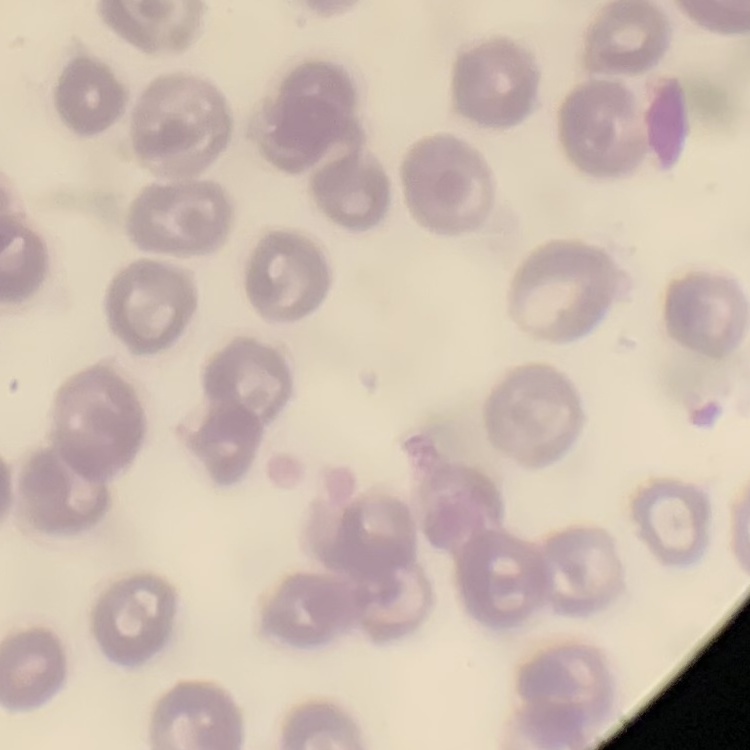

The red blood cells exhibit no rouleaux formation. Field's or Giemsa stain. Thin blood smear. One tile cut from a larger photomicrograph.